Describe the morphology of the erythrocytes.
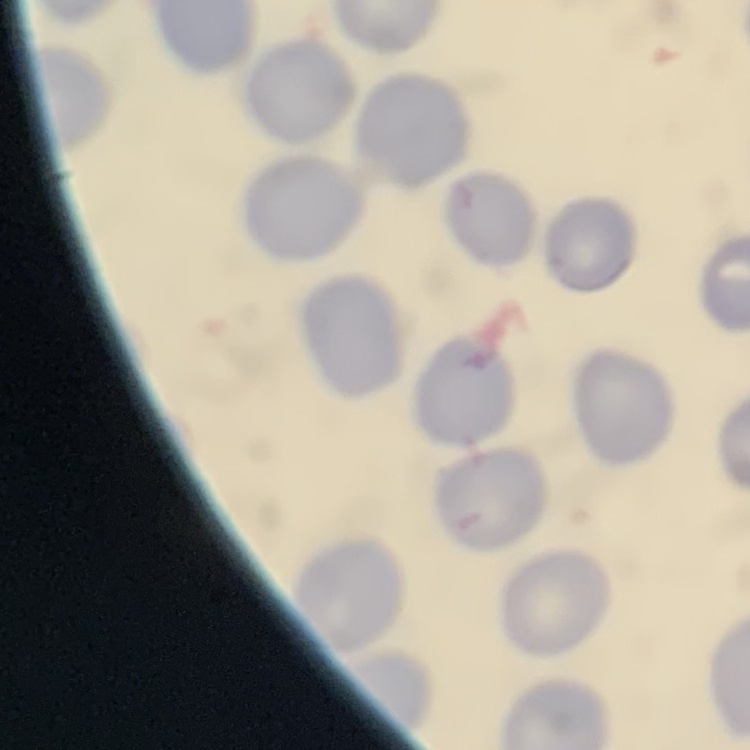
No rouleaux formation.

image_type: one tile cut from a larger photomicrograph
stain: Field's or Giemsa
preparation: thin blood smear